Classify this cell by malaria status.
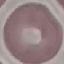

Uninfected.

capture: smartphone camera at the microscope eyepiece
stain: Giemsa
preparation: thin blood film
image_type: cell patch, automatically extracted from a larger field of view and resized to 64 × 64 pixels